Point out each Plasmodium parasite.
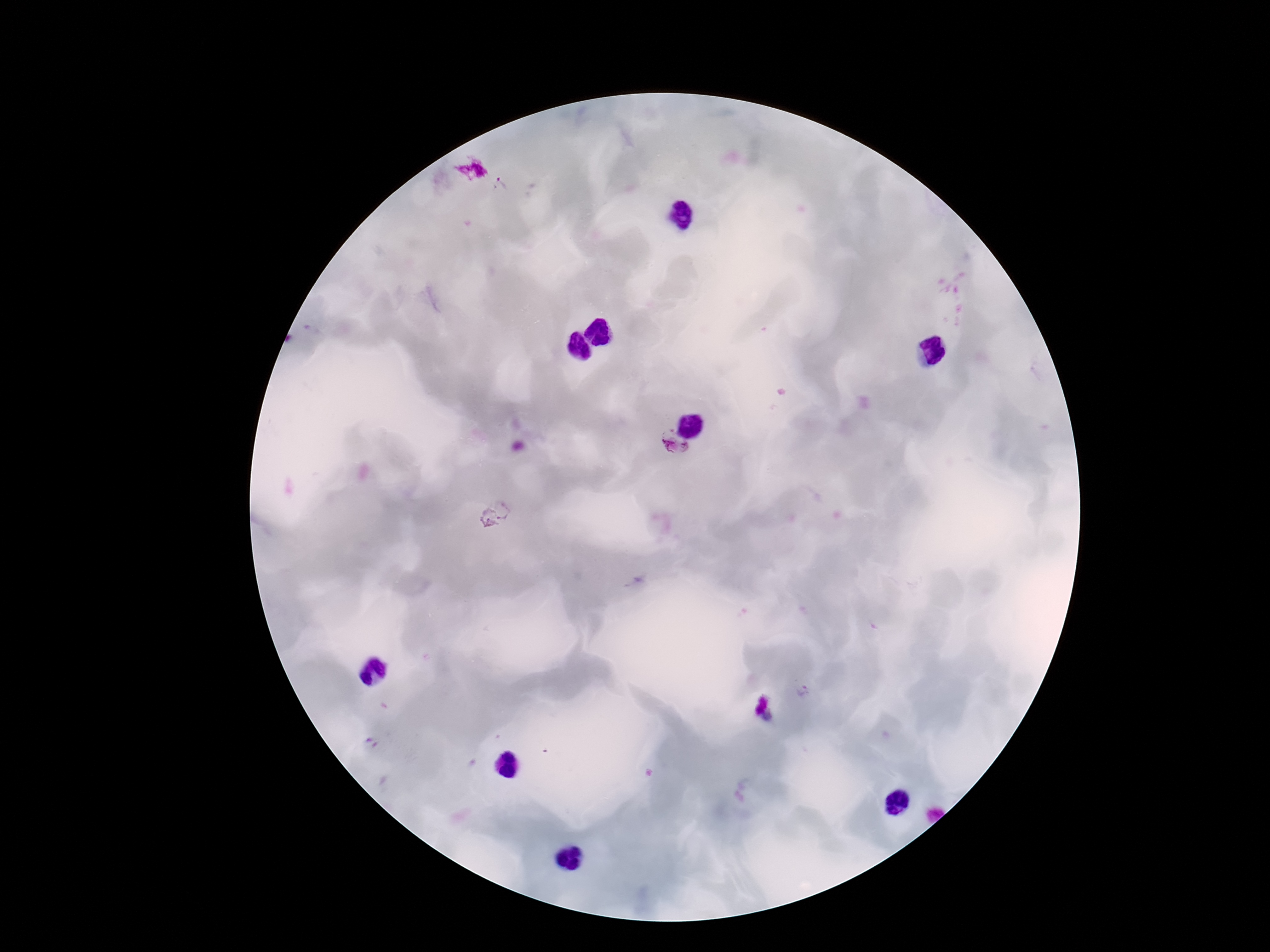

Approximate centers as {x, y} in pixels.
Plasmodium parasites: {500, 187}, {674, 450}, {505, 508}, {487, 519}, {804, 693}.

Image is 1270×952 pixels. Single field of view. Patient malaria status: infected. Giemsa-stained preparation. 100x magnification. Smartphone photograph taken through the microscope eyepiece. Thick peripheral-blood smear.